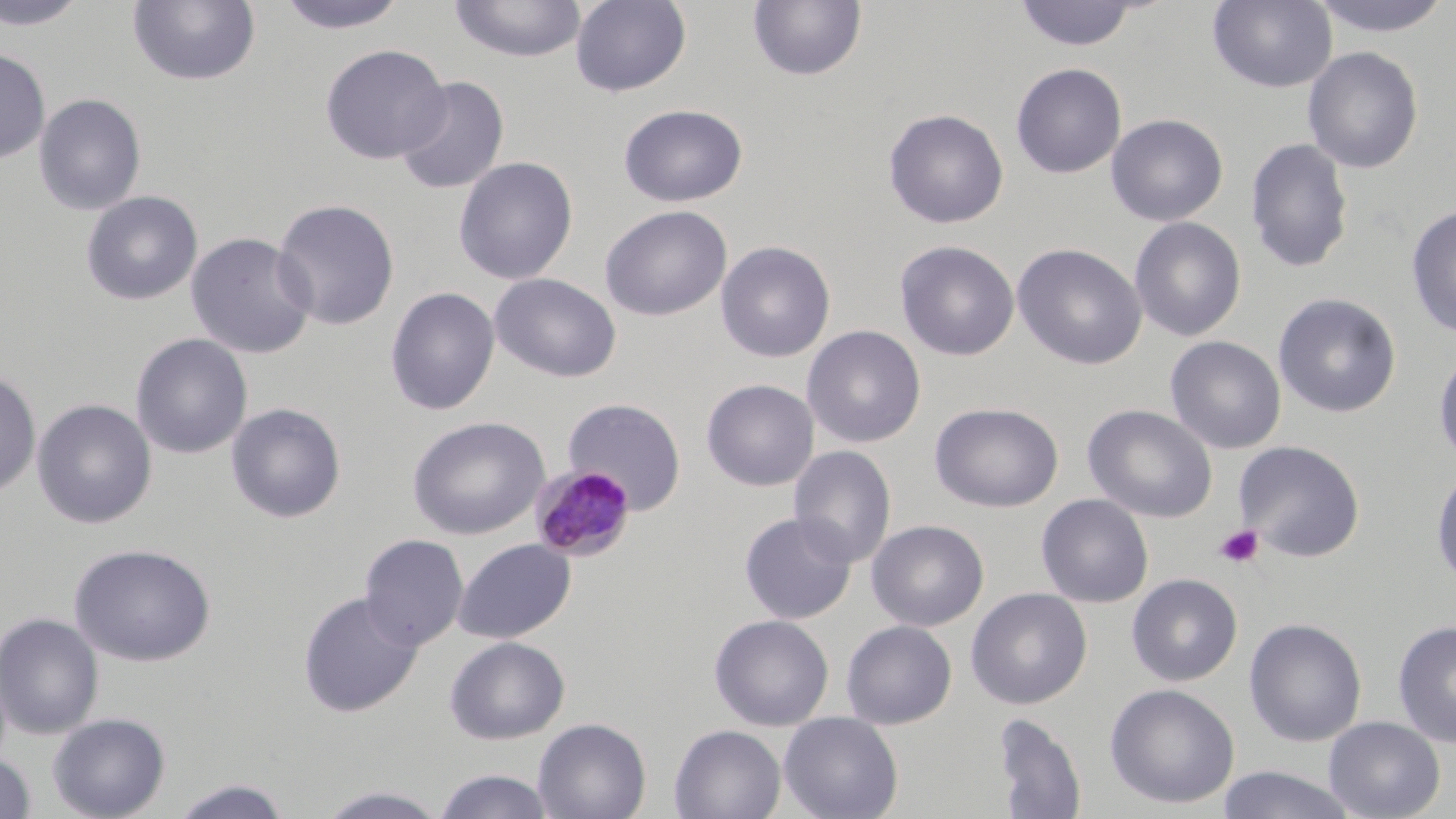 Approximate bounding boxes as named x1/y1/x2/y2 corners in pixels. Platelet locations: (x1=1214, y1=524, x2=1264, y2=569). Plasmodium malariae-infected red blood cell locations: (x1=530, y1=464, x2=636, y2=562). Uninfected red blood cell locations: (x1=0, y1=0, x2=90, y2=31), (x1=275, y1=0, x2=409, y2=34), (x1=448, y1=0, x2=588, y2=63), (x1=570, y1=0, x2=692, y2=97), (x1=1207, y1=0, x2=1337, y2=93), (x1=1305, y1=0, x2=1455, y2=38), (x1=127, y1=1, x2=261, y2=87), (x1=747, y1=1, x2=867, y2=82), (x1=1014, y1=1, x2=1142, y2=51), (x1=319, y1=43, x2=451, y2=164), (x1=1302, y1=46, x2=1423, y2=174), (x1=0, y1=47, x2=50, y2=165), (x1=1011, y1=62, x2=1127, y2=179), (x1=394, y1=76, x2=509, y2=195), (x1=34, y1=93, x2=147, y2=215), (x1=618, y1=103, x2=748, y2=207), (x1=883, y1=108, x2=1008, y2=229), (x1=1106, y1=113, x2=1228, y2=226), (x1=1245, y1=138, x2=1354, y2=273), (x1=453, y1=156, x2=578, y2=285), (x1=81, y1=190, x2=203, y2=306), (x1=272, y1=199, x2=400, y2=330), (x1=600, y1=205, x2=731, y2=321), (x1=1405, y1=205, x2=1456, y2=339), (x1=1129, y1=217, x2=1247, y2=342), (x1=185, y1=232, x2=317, y2=359), (x1=715, y1=240, x2=835, y2=362), (x1=895, y1=240, x2=1019, y2=361), (x1=1012, y1=243, x2=1147, y2=370), (x1=489, y1=272, x2=622, y2=382), (x1=385, y1=287, x2=500, y2=415), (x1=1273, y1=293, x2=1401, y2=418), (x1=802, y1=325, x2=926, y2=448), (x1=131, y1=333, x2=253, y2=459), (x1=1165, y1=336, x2=1286, y2=454), (x1=1432, y1=345, x2=1456, y2=469), (x1=0, y1=369, x2=41, y2=499), (x1=701, y1=378, x2=819, y2=491), (x1=562, y1=397, x2=687, y2=514), (x1=32, y1=398, x2=157, y2=528), (x1=226, y1=402, x2=346, y2=523), (x1=930, y1=402, x2=1064, y2=513), (x1=1083, y1=404, x2=1217, y2=522), (x1=407, y1=415, x2=550, y2=540), (x1=1233, y1=440, x2=1365, y2=562), (x1=788, y1=445, x2=896, y2=568), (x1=1430, y1=466, x2=1456, y2=588), (x1=1036, y1=494, x2=1154, y2=608), (x1=739, y1=512, x2=857, y2=625), (x1=867, y1=519, x2=989, y2=632), (x1=359, y1=533, x2=469, y2=650), (x1=453, y1=538, x2=576, y2=644), (x1=69, y1=543, x2=216, y2=666), (x1=1127, y1=573, x2=1243, y2=687), (x1=966, y1=588, x2=1092, y2=709), (x1=298, y1=591, x2=423, y2=717), (x1=0, y1=612, x2=104, y2=739), (x1=709, y1=614, x2=834, y2=731), (x1=1244, y1=617, x2=1367, y2=747), (x1=841, y1=620, x2=957, y2=729), (x1=1392, y1=620, x2=1456, y2=749), (x1=445, y1=636, x2=570, y2=744), (x1=1104, y1=683, x2=1240, y2=809), (x1=779, y1=711, x2=903, y2=819), (x1=47, y1=712, x2=170, y2=819), (x1=991, y1=712, x2=1087, y2=819), (x1=1323, y1=716, x2=1445, y2=819), (x1=533, y1=717, x2=651, y2=819), (x1=669, y1=724, x2=786, y2=819), (x1=0, y1=753, x2=36, y2=818), (x1=1215, y1=766, x2=1359, y2=819), (x1=433, y1=769, x2=556, y2=818), (x1=167, y1=778, x2=294, y2=818), (x1=314, y1=784, x2=452, y2=818). Slide-level diagnosis: Plasmodium malariae. May-Grünwald-Giemsa stain. Captured at 1000x magnification. Thin blood film. One field of a larger specimen. Light microscopy. Image is 1456×819 pixels.